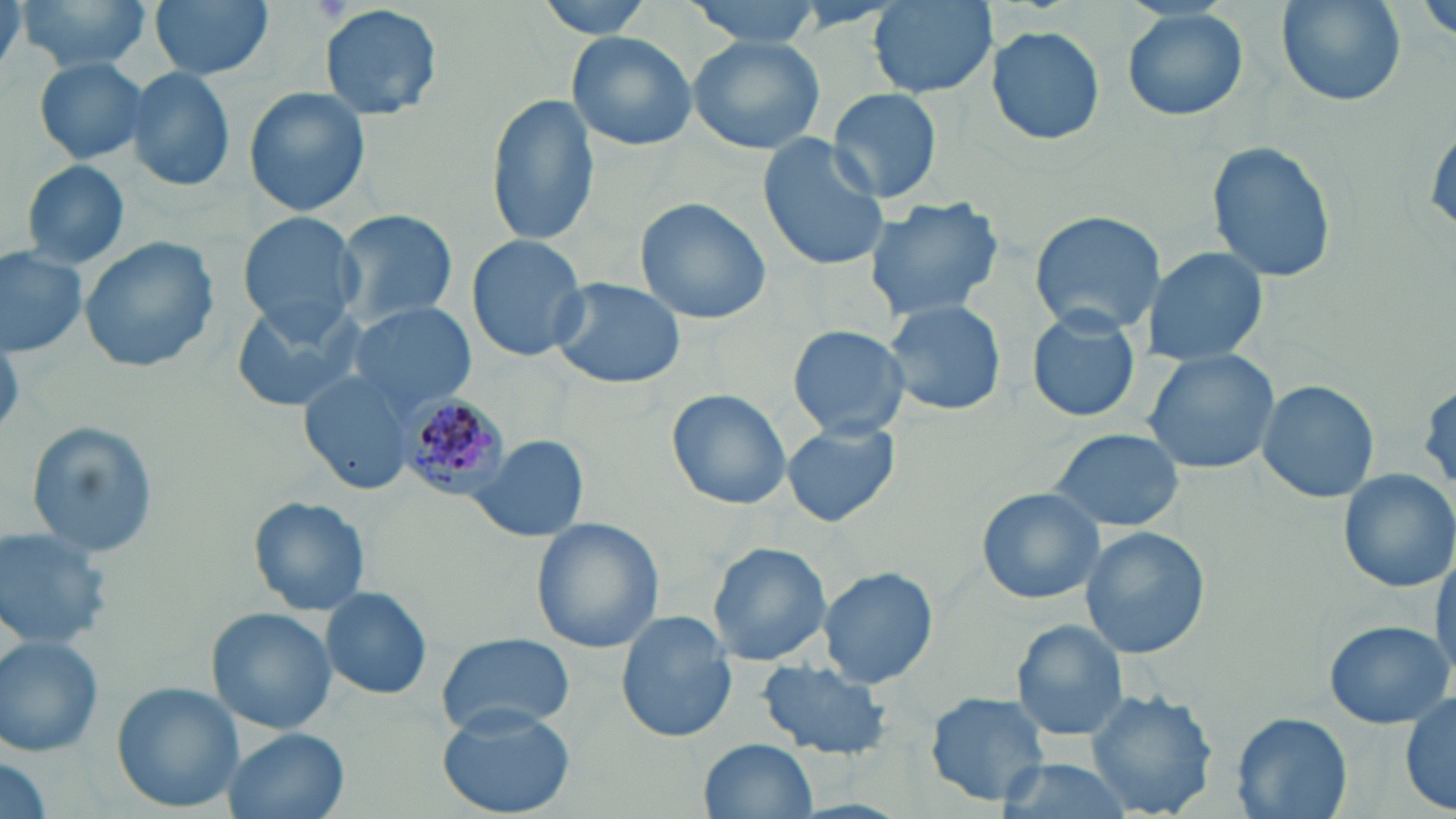
Approximate bounding boxes as [x1, y1, x2, y2] in pixels. Plasmodium malariae-infected red blood cell locations: [397, 390, 512, 499]. Uninfected red blood cell locations: [16, 0, 151, 72], [150, 0, 275, 81], [535, 0, 663, 37], [685, 0, 827, 47], [1276, 0, 1406, 108], [1418, 0, 1456, 43], [0, 1, 27, 82], [871, 2, 996, 98], [320, 3, 442, 122], [1121, 9, 1249, 122], [987, 25, 1105, 146], [565, 31, 697, 152], [688, 34, 827, 156], [33, 57, 151, 165], [125, 65, 235, 193], [243, 87, 372, 217], [827, 88, 944, 204], [486, 92, 600, 248], [758, 135, 890, 272], [1206, 138, 1337, 286], [20, 159, 132, 271], [862, 192, 1009, 320], [634, 197, 771, 324], [334, 208, 460, 326], [1026, 209, 1167, 334], [235, 212, 364, 337], [466, 235, 589, 361], [79, 236, 218, 373], [1140, 245, 1271, 367], [0, 248, 89, 360], [547, 277, 686, 390], [881, 297, 1007, 419], [231, 298, 368, 414], [348, 304, 477, 414], [1025, 308, 1141, 423], [789, 326, 910, 437], [1142, 349, 1284, 474], [300, 371, 420, 493], [1256, 379, 1380, 503], [666, 388, 792, 510], [782, 419, 901, 528], [26, 422, 160, 559], [1045, 427, 1185, 533], [471, 434, 588, 544], [1335, 467, 1456, 593], [976, 486, 1109, 605], [249, 496, 372, 616], [533, 518, 663, 654], [1079, 525, 1211, 660], [0, 527, 113, 651], [709, 542, 834, 667], [1430, 549, 1455, 688], [818, 567, 938, 688], [321, 586, 433, 699], [207, 608, 337, 735], [617, 611, 736, 743], [1012, 618, 1129, 742], [1323, 619, 1452, 729], [435, 631, 577, 738], [0, 634, 106, 758], [758, 657, 893, 760], [113, 681, 242, 811], [1085, 688, 1222, 818], [1400, 688, 1456, 815], [924, 691, 1052, 807], [437, 704, 576, 817], [1232, 712, 1353, 819], [223, 728, 351, 819], [701, 737, 819, 819], [2, 754, 50, 819], [991, 758, 1135, 819]. Slide-level diagnosis: Plasmodium malariae. May-Grünwald-Giemsa stain. Image is 1456×819 pixels. Thin blood smear. Optical microscopy. Captured at 1000x magnification. Single field of view.